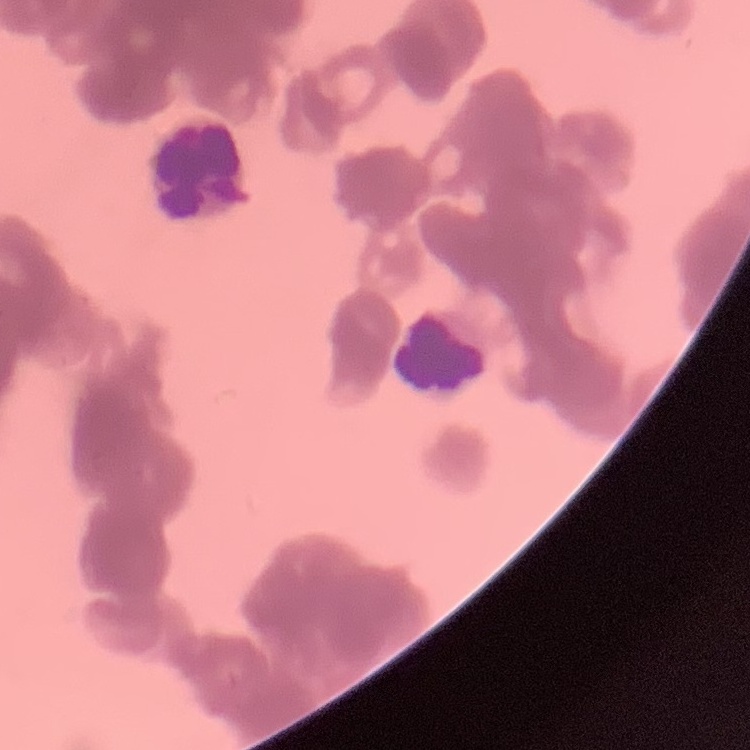
Summary:
  - Erythrocyte morphology: rouleaux formation
  - Image type: one tile cut from a larger photomicrograph
  - Stain: Field's or Giemsa
  - Preparation: thin peripheral smear